Describe the morphology of the red blood cells.
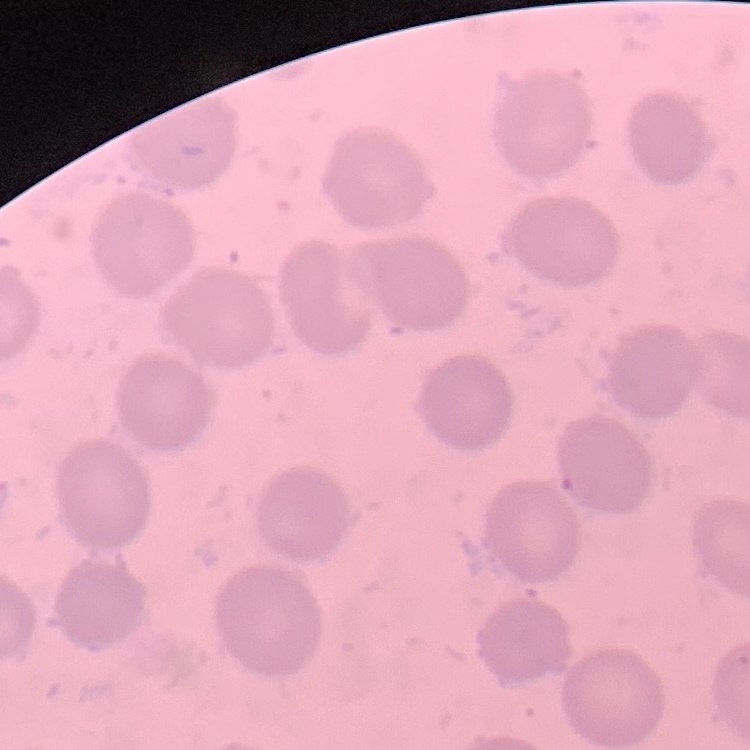
They show no rouleaux formation.

preparation = thin blood smear
image type = one tile cut from a larger photomicrograph
stain = Field's or Giemsa